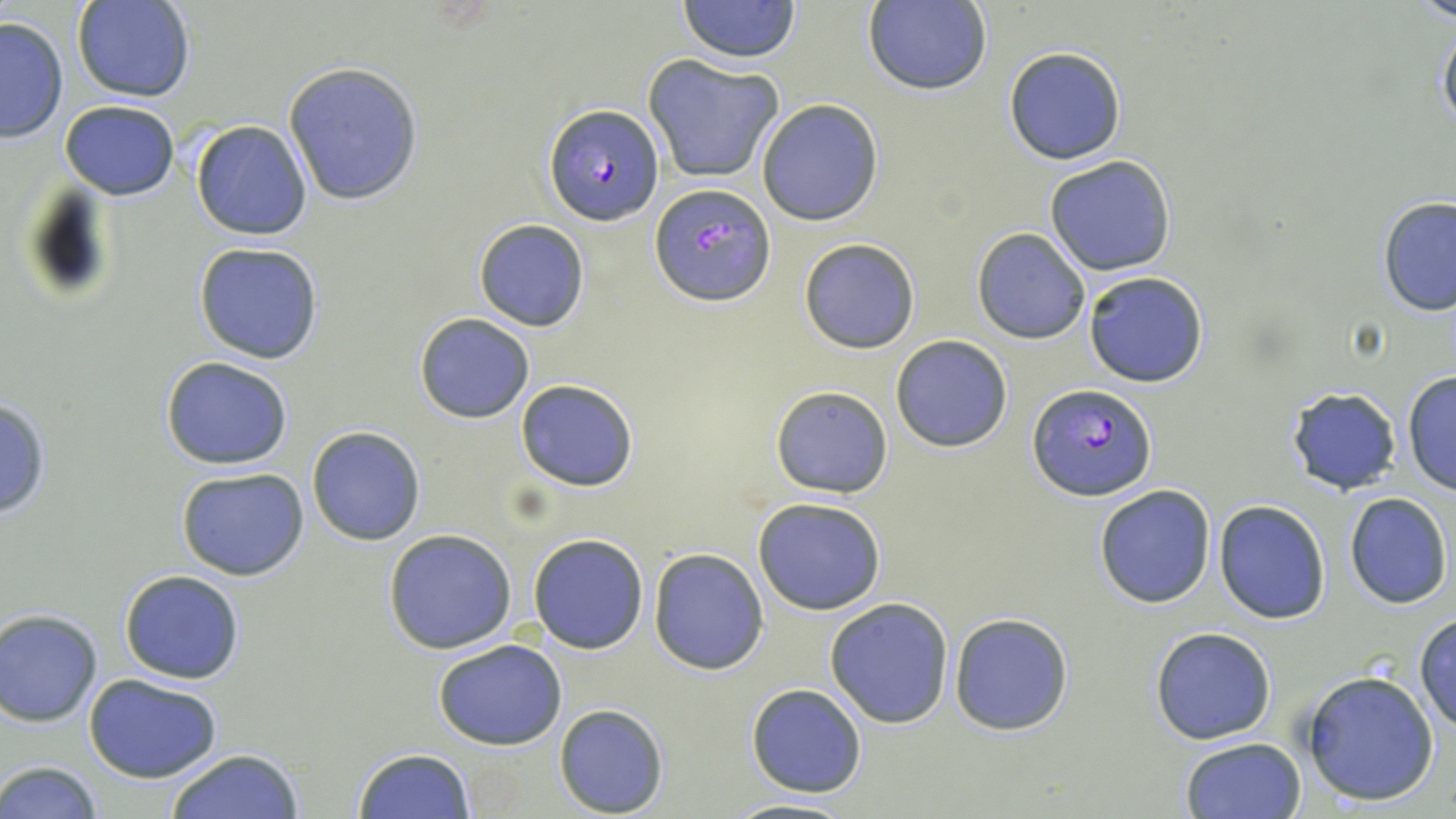

{
  "slide_level_diagnosis": "Plasmodium falciparum",
  "preparation": "thin blood smear",
  "field_of_view": "single",
  "plasmodium_falciparum_infected_red_blood_cell_locations": "approximate bounding boxes as (x1,y1)-(x2,y2) corner pairs in pixels: (544,104)-(663,226), (652,184)-(776,305), (1029,383)-(1156,501)",
  "magnification": "1000x",
  "stain": "May-Grünwald-Giemsa",
  "image_size": "1456×819 pixels",
  "uninfected_red_blood_cell_locations": "approximate bounding boxes as (x1,y1)-(x2,y2) corner pairs in pixels: (73,0)-(196,102), (677,0)-(801,64), (864,0)-(993,97), (1413,0)-(1456,24), (0,16)-(69,141), (1437,17)-(1456,141), (1002,46)-(1127,165), (644,55)-(784,183), (283,62)-(422,206), (756,99)-(885,226), (60,100)-(179,200), (191,119)-(311,241), (1045,155)-(1177,276), (1376,196)-(1456,316), (473,219)-(591,332), (971,227)-(1090,344), (799,238)-(920,352), (193,242)-(324,365), (1083,271)-(1211,388), (414,313)-(535,423), (889,335)-(1013,453), (161,356)-(293,470), (1401,371)-(1456,496), (515,379)-(639,492), (769,384)-(894,498), (1282,386)-(1402,496), (0,398)-(53,521), (305,425)-(426,545), (175,467)-(309,581), (1093,483)-(1216,609), (1344,493)-(1452,609), (752,496)-(886,614), (1214,499)-(1330,623), (384,528)-(517,653), (529,532)-(649,654), (649,548)-(769,676), (120,569)-(245,685), (824,598)-(954,729), (0,608)-(103,726), (949,611)-(1075,736), (1413,615)-(1456,732), (1150,627)-(1277,745), (433,639)-(567,750), (1300,671)-(1440,806), (84,675)-(223,784), (745,682)-(869,797), (554,703)-(670,817), (1180,735)-(1307,819), (351,747)-(475,819), (165,748)-(306,819), (0,761)-(103,819), (724,796)-(860,819)",
  "modality": "light microscopy"
}